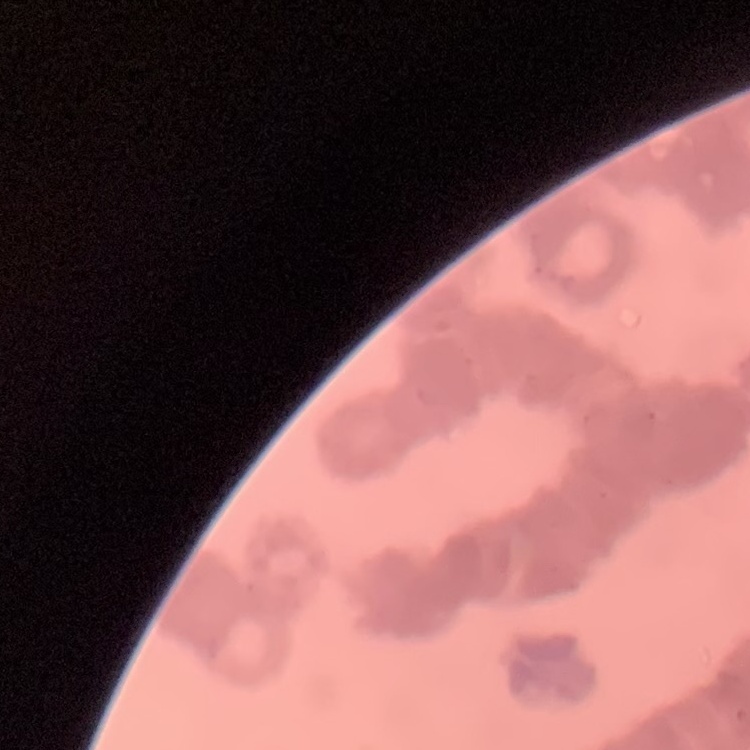
{
  "red_blood_cell_morphology": "rouleaux formation",
  "preparation": "thin blood smear",
  "image_type": "one tile cut from a larger photomicrograph",
  "stain": "Field's or Giemsa"
}